Identify the blood parasite species.
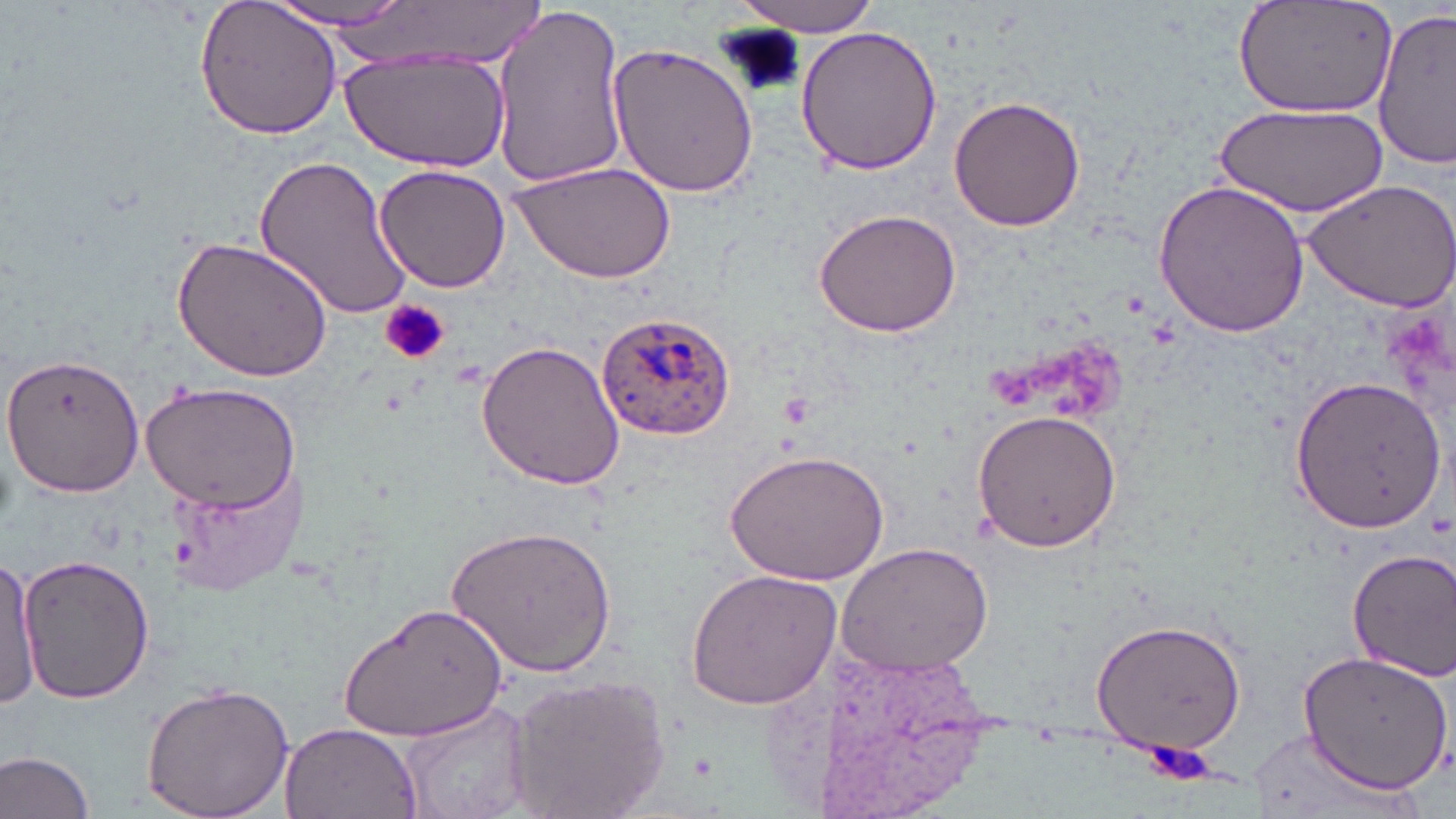
Plasmodium ovale.

Summary:
  - Coordinate format: approximate bounding boxes as (x1,y1)-(x2,y2) corner pairs in pixels
  - Platelet locations: (719,25)-(806,99), (380,297)-(448,366), (1146,739)-(1215,787)
  - Uninfected red blood cell locations: (194,0)-(345,139), (734,0)-(882,35), (1231,0)-(1396,119), (261,2)-(422,34), (486,5)-(630,190), (1373,9)-(1454,169), (794,24)-(943,177), (607,40)-(759,201), (341,52)-(509,173), (948,94)-(1087,233), (1216,102)-(1390,216), (251,153)-(417,322), (511,158)-(673,283), (375,163)-(514,293), (1301,177)-(1456,314), (1150,178)-(1313,339), (810,207)-(962,339), (173,236)-(335,383), (475,338)-(627,492), (0,354)-(148,497), (1288,375)-(1446,533), (141,381)-(303,514), (969,408)-(1123,552), (725,447)-(892,584), (167,463)-(302,597), (449,522)-(620,678), (838,540)-(996,676), (1346,547)-(1456,681), (18,553)-(155,705), (0,556)-(40,713), (685,567)-(841,712), (341,604)-(511,743), (1089,616)-(1250,756), (1290,647)-(1450,798), (501,671)-(668,819), (140,680)-(296,819), (398,702)-(531,819), (278,721)-(423,819), (1249,727)-(1402,819), (0,748)-(99,819)
  - Plasmodium ovale-infected red blood cell locations: (595,310)-(736,439)
  - Modality: light microscopy
  - Magnification: 1000x
  - Image size: 1456×819 pixels
  - Preparation: thin blood smear
  - Field of view: single
  - Stain: May-Grünwald-Giemsa